Point out each Plasmodium parasite.
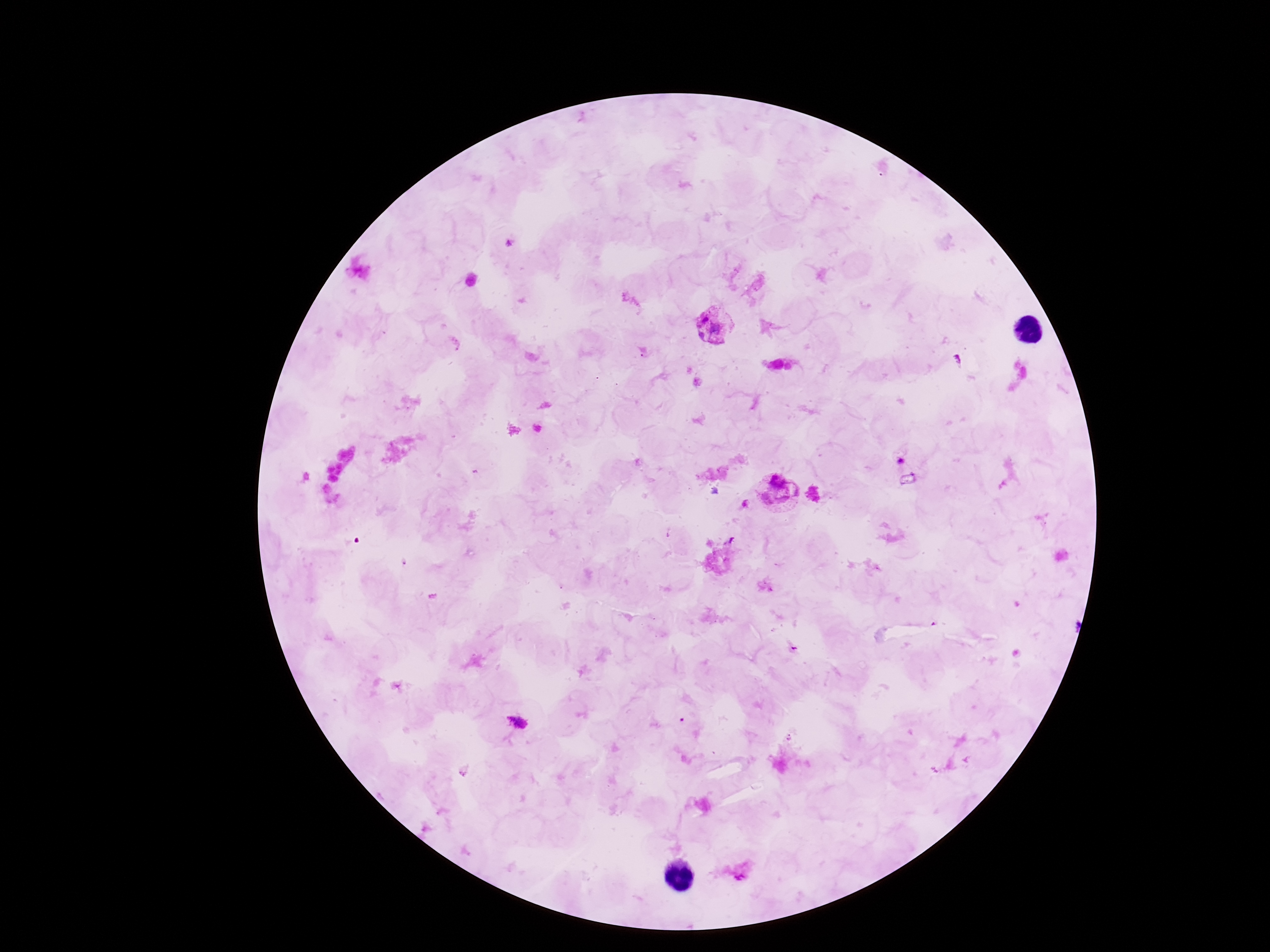
Approximate centers as {x, y} in pixels.
Plasmodium parasites: {718, 327}, {901, 460}, {777, 496}, {516, 723}, {741, 871}.

patient malaria status = infected
image size = 1270×952 pixels
preparation = thick blood film
capture = smartphone camera through the microscope eyepiece
field of view = single
magnification = 100x
stain = Giemsa